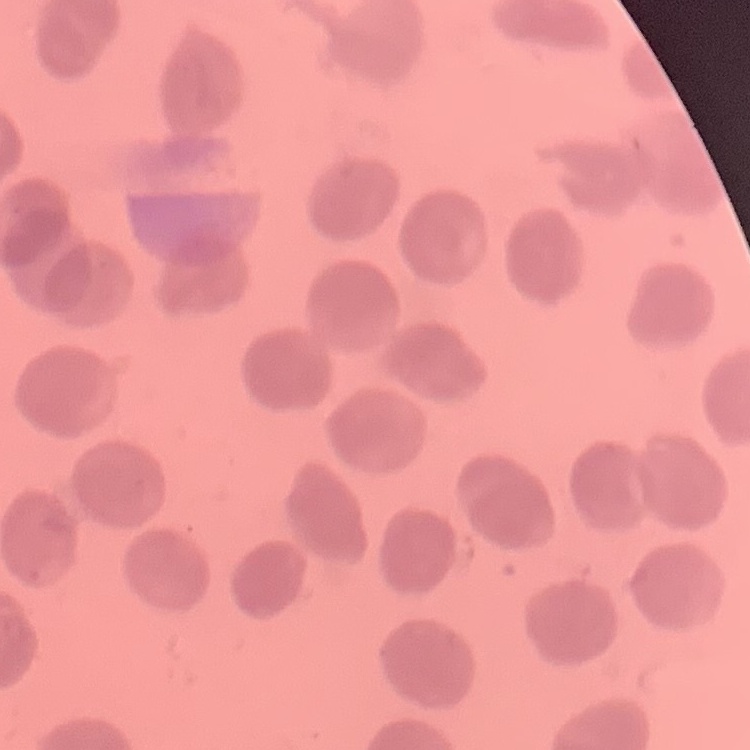

erythrocyte_morphology: no rouleaux formation
preparation: thin peripheral smear
stain: Field's or Giemsa
image_type: square crop of a larger photomicrograph